Assess this cell for malaria.
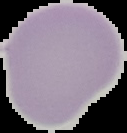
It is uninfected.

image type = cell region segmented out of the field of view; surrounding area masked to black
image size = 127×133 pixels
preparation = thin blood film